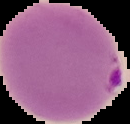

From a thin blood smear. Image is 130×124 pixels. Malaria status: parasitized. Cell region segmented out of the field of view; the surrounding area is masked to black.